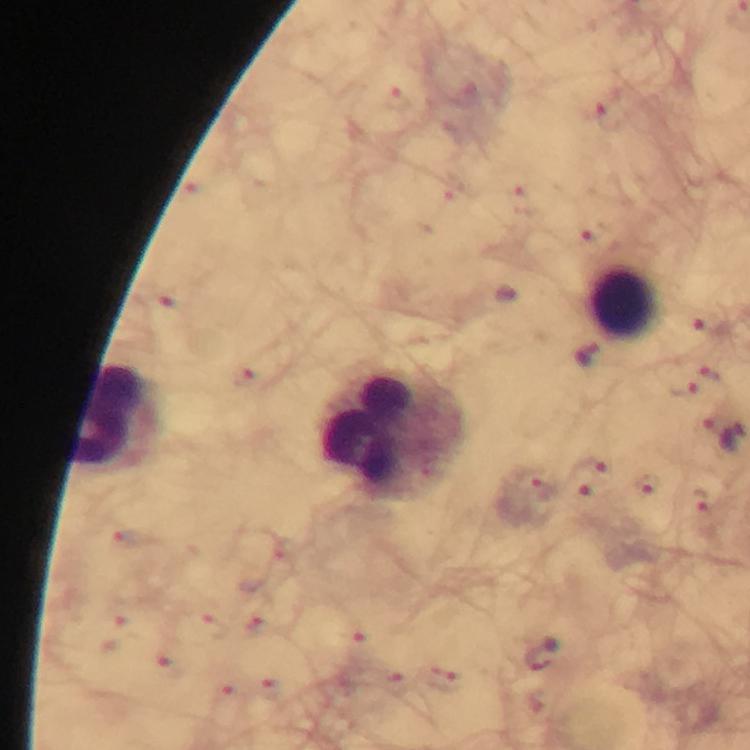
stain = Giemsa
preparation = thick blood smear
cropped from = a single field of view
magnification = 100x
immersion oil = used
malaria parasite locations = approximate object centers, in pixels from the top-left corner: (x=608, y=117), (x=706, y=326), (x=714, y=374), (x=683, y=390), (x=592, y=466), (x=645, y=484), (x=541, y=487), (x=588, y=498), (x=700, y=500), (x=542, y=654)
capture = smartphone photograph through a microscope
leukocyte locations = approximate object centers, in pixels from the top-left corner: (x=623, y=305), (x=114, y=418), (x=393, y=436)
image size = 750×750 pixels
context = from a diagnostic examination for malaria